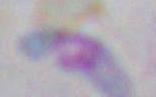

Photomicrograph. Toxoplasma gondii is shown. 1000x magnification.